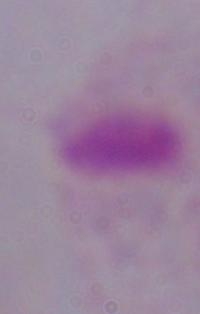

Photomicrograph. 1000x magnification. A trichomonad is seen.